State which parasite is depicted.
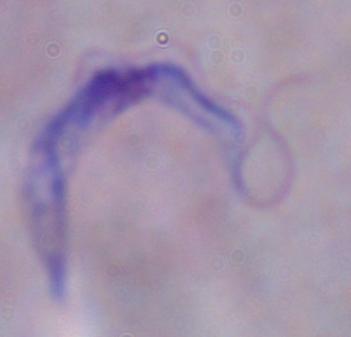
This is a trypanosome.

Summary:
  - Magnification: 1000x
  - Modality: photomicrograph